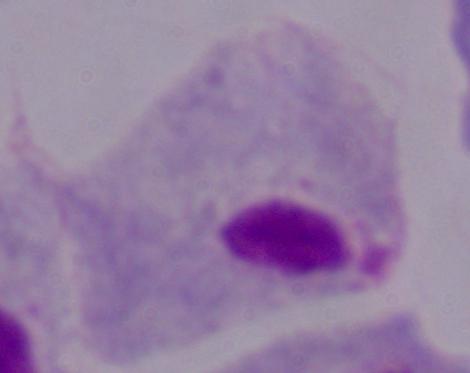 Micrograph. Captured at 1000x magnification. A trichomonad is shown.